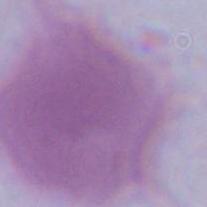
Micrograph. Captured at 1000x magnification. A red blood cell is seen.